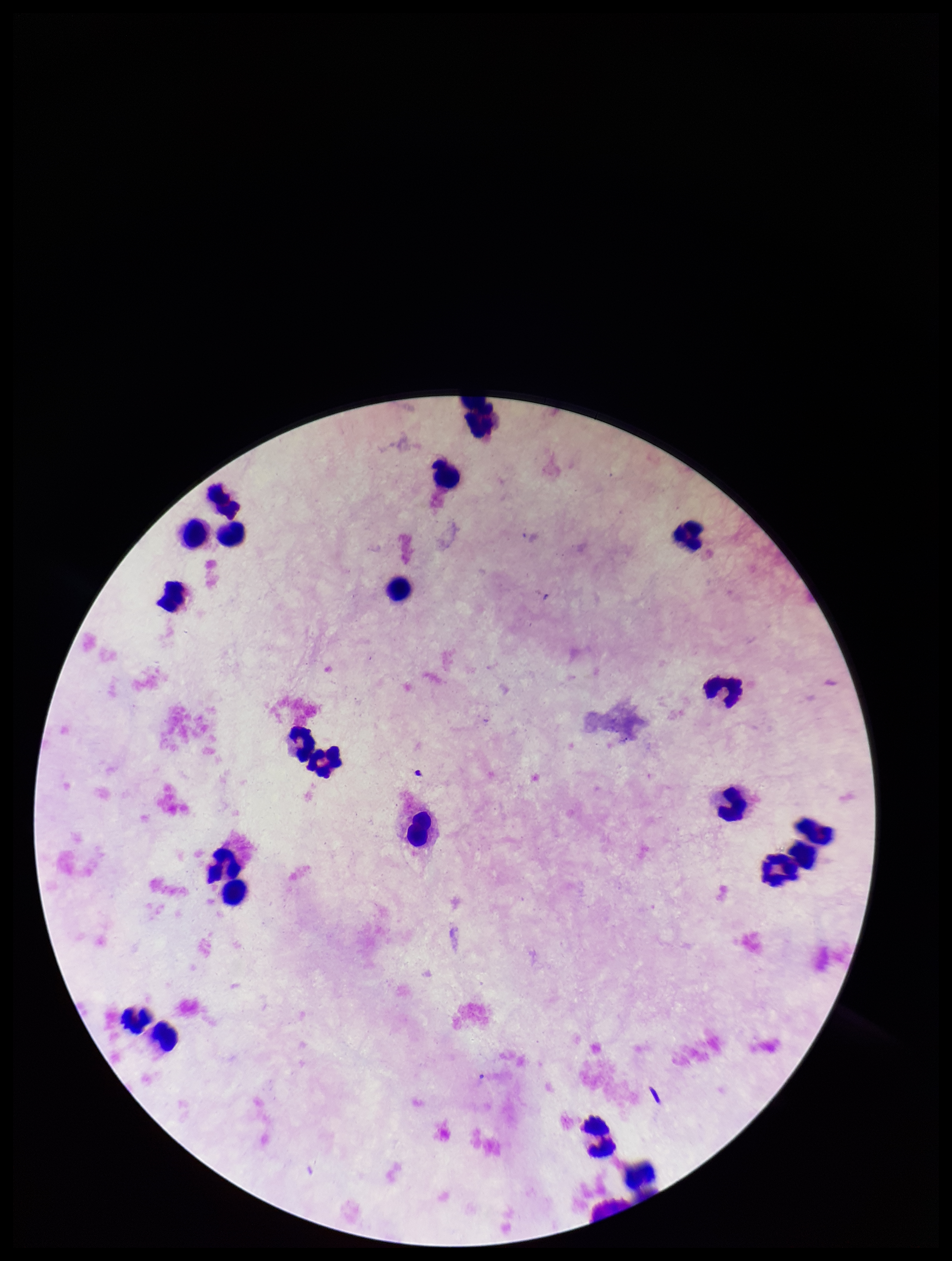

Stained with Giemsa. Plasmodium parasites: none detected. Smartphone photograph taken through the eyepiece of a microscope. Patient malaria status: negative. Parasite count: 0. Preparation: thick blood smear. One field from this slide. Leukocyte count: 22. Image is 952×1261 pixels.